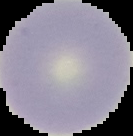
Cell region segmented out of the field of view; the surrounding area is masked to black. Malaria status: uninfected. Image is 133×136 pixels. From a thin blood smear.